Locate every parasitized RBC.
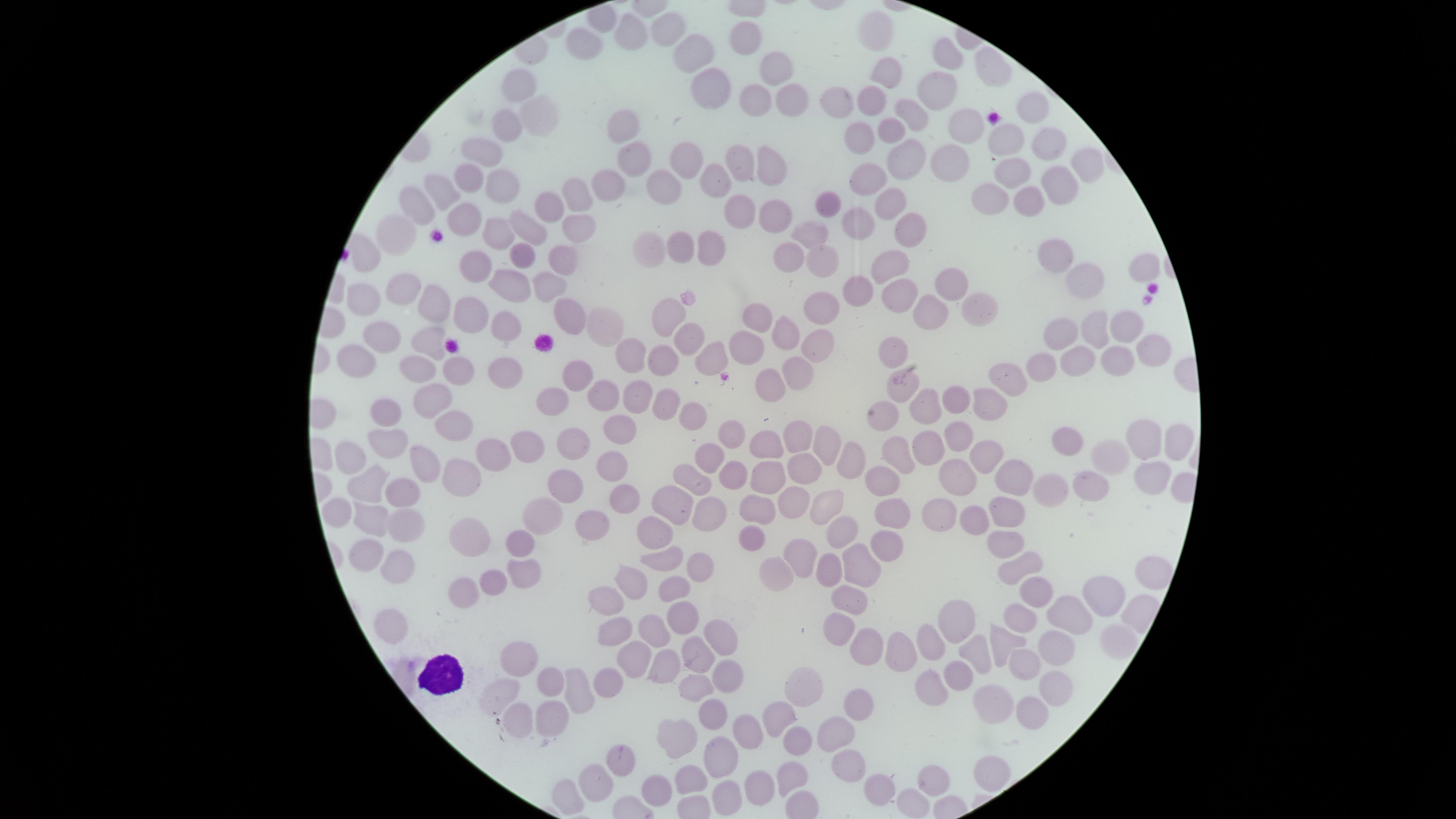

No parasitized RBCs identified.

field of view = single
visible region = circular
image size = 1456×819 pixels
capture = smartphone photograph through the microscope eyepiece
preparation = thin blood film
stain = Giemsa
uninfected RBCs = approximate marker points as [x, y] in pixels: [671, 24], [630, 28], [878, 30], [587, 33], [745, 35], [692, 46], [942, 54], [778, 67], [988, 69], [885, 73], [934, 81], [523, 82], [702, 84], [871, 93], [753, 97], [790, 99], [841, 101], [909, 108], [1032, 109], [540, 115], [624, 118], [890, 122], [505, 123], [966, 125], [860, 132], [1007, 139], [1047, 143], [480, 146], [685, 152], [739, 158], [635, 159], [906, 161], [768, 162], [950, 163], [1005, 163], [1084, 164], [474, 173], [500, 179], [870, 179], [609, 181], [709, 181], [1060, 181], [660, 182], [445, 187], [986, 193], [572, 194], [1024, 196], [827, 199], [890, 200], [554, 206], [422, 207], [740, 208], [769, 211], [464, 216], [856, 219], [578, 223], [495, 228], [528, 228], [906, 230], [393, 235], [810, 241], [676, 243], [645, 250], [711, 250], [518, 251], [1056, 254], [562, 255], [782, 255], [821, 260], [889, 260], [474, 261], [1136, 270], [1080, 281], [543, 282], [954, 282], [506, 283], [856, 288], [403, 289], [892, 292], [434, 302], [362, 303], [974, 305], [821, 309], [468, 312], [566, 312], [752, 312], [929, 312], [665, 316], [502, 323], [598, 323], [1119, 325], [782, 326], [1093, 328], [1061, 333], [424, 334], [687, 334], [376, 335], [813, 338], [1145, 344], [745, 349], [894, 349], [630, 351], [357, 357], [658, 357], [1124, 360], [703, 364], [1077, 364], [415, 365], [455, 366], [508, 366], [1041, 368], [574, 370], [1011, 372], [796, 373], [767, 382], [630, 388], [598, 393], [436, 394], [551, 397], [989, 397], [950, 398], [667, 403], [921, 403], [690, 407], [378, 408], [448, 418], [623, 429], [798, 432], [960, 434], [734, 436], [1068, 437], [393, 439], [1136, 439], [1177, 439], [823, 440], [573, 441], [765, 442], [920, 442], [526, 448], [901, 449], [497, 451], [1107, 455], [354, 456], [710, 456], [427, 457], [844, 457], [991, 457], [611, 458], [466, 468], [732, 471], [803, 471], [953, 473], [695, 475], [1023, 475], [1155, 477], [765, 478], [376, 479], [878, 481], [565, 482], [1096, 482], [1059, 487], [407, 488], [621, 491], [789, 502], [677, 503], [830, 503], [344, 507], [760, 507], [945, 511], [889, 513], [711, 514], [1003, 515], [539, 518], [974, 518], [372, 519], [403, 524], [589, 524], [839, 528], [657, 533], [750, 536], [519, 539], [469, 540], [1008, 543], [884, 544], [370, 550], [799, 551], [665, 556], [393, 560], [860, 561], [1019, 564], [699, 566], [519, 569], [774, 571], [831, 572], [1148, 574], [485, 577], [634, 579], [678, 586], [463, 588], [1103, 594], [1033, 596], [854, 597], [607, 598], [677, 609], [1025, 611], [1071, 611], [963, 618], [391, 623], [832, 624], [654, 627], [619, 629], [719, 635], [1060, 636], [935, 637], [1011, 639], [871, 645], [702, 648], [980, 651], [910, 654], [634, 655], [524, 657], [1019, 664], [662, 666], [730, 671], [956, 673], [609, 677], [552, 680], [801, 683], [929, 684], [1057, 686], [703, 687], [503, 692], [576, 693], [853, 701], [988, 703], [720, 705], [1029, 707], [548, 716], [775, 718], [518, 723], [747, 728], [833, 730], [672, 731], [793, 744], [619, 757], [723, 759], [845, 766], [988, 768], [787, 772], [593, 779], [931, 779], [685, 780], [763, 781], [884, 784], [656, 786], [732, 792]
WBCs = approximate marker points as [x, y] in pixels: [435, 675]